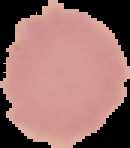

Malaria status: uninfected. From a thin blood smear. Segmented cell region on a black background. Image is 130×148 pixels.